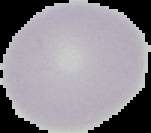
{
  "image_type": "segmented cell region on a black background",
  "malaria_status": "uninfected",
  "preparation": "thin blood film",
  "image_size": "151×133 pixels"
}